Assess the morphology of the red blood cells.
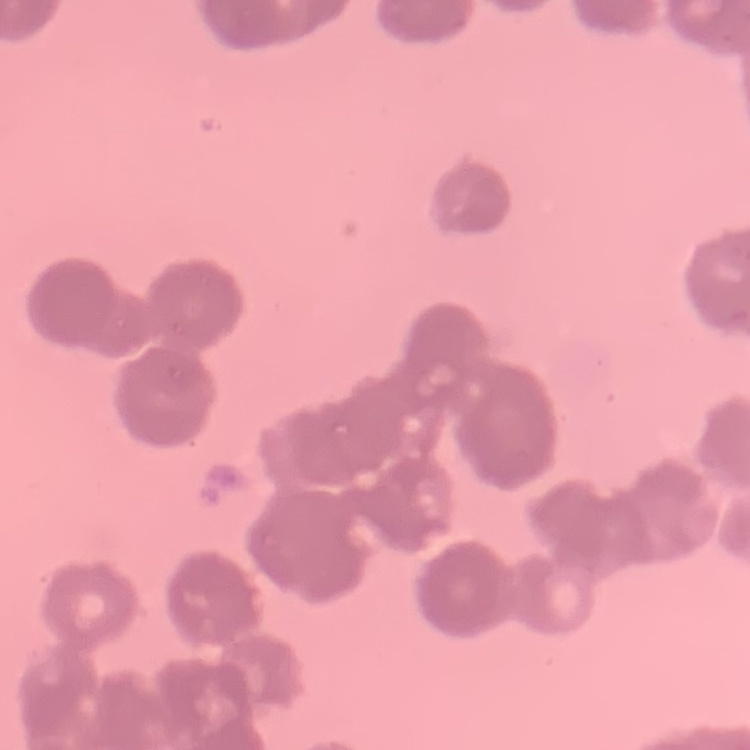
They show rouleaux formation.

Stained with either Field's or Giemsa. Thin peripheral smear. Square crop of a larger photomicrograph.